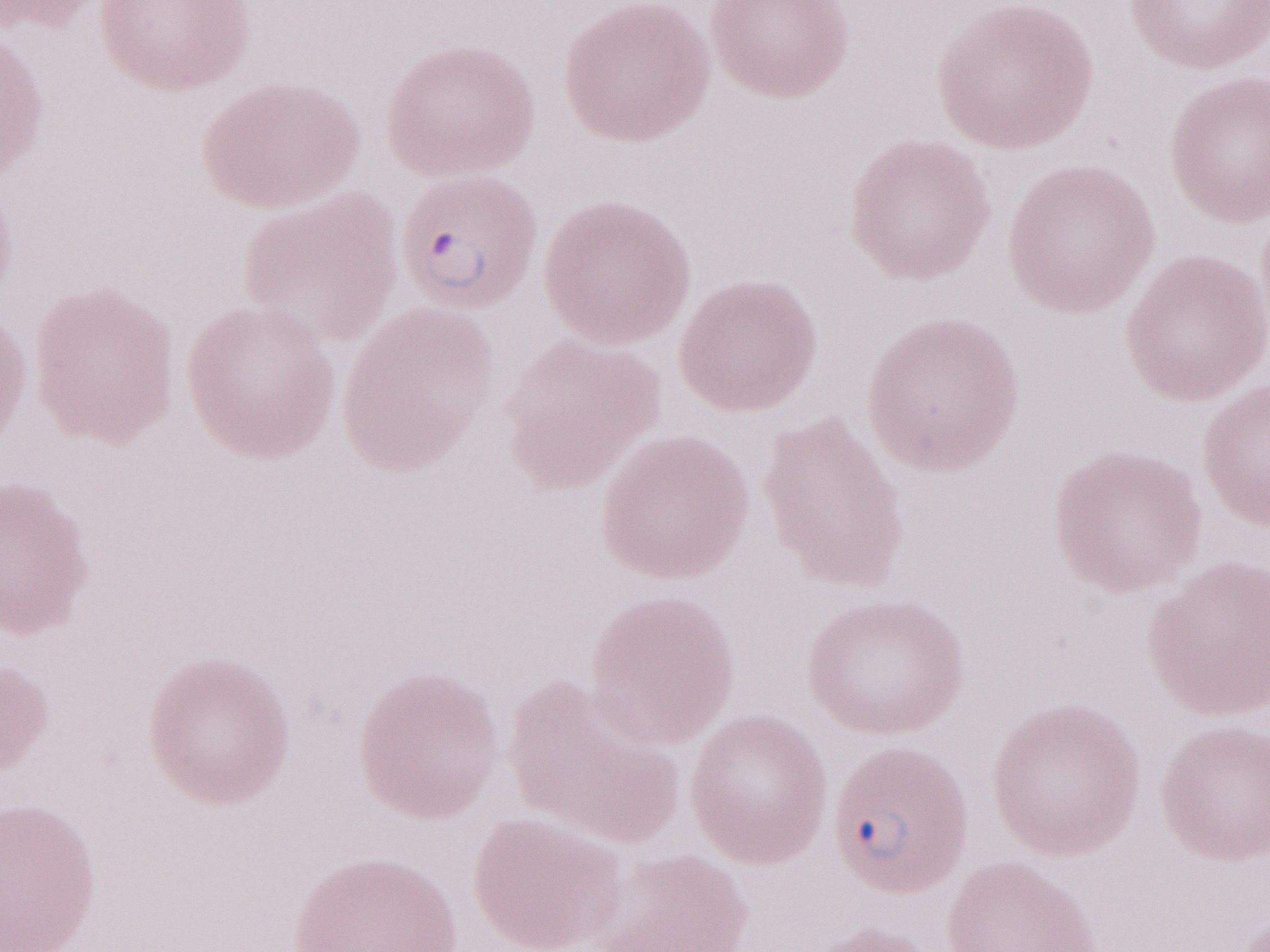

Image is 1270×952 pixels. Thin peripheral-blood smear. May-Grünwald-Giemsa stain. Patient-level malaria diagnosis: positive. Single field of view. Olympus BX43 microscope, Olympus DP73 camera. Magnification: 1,000x.